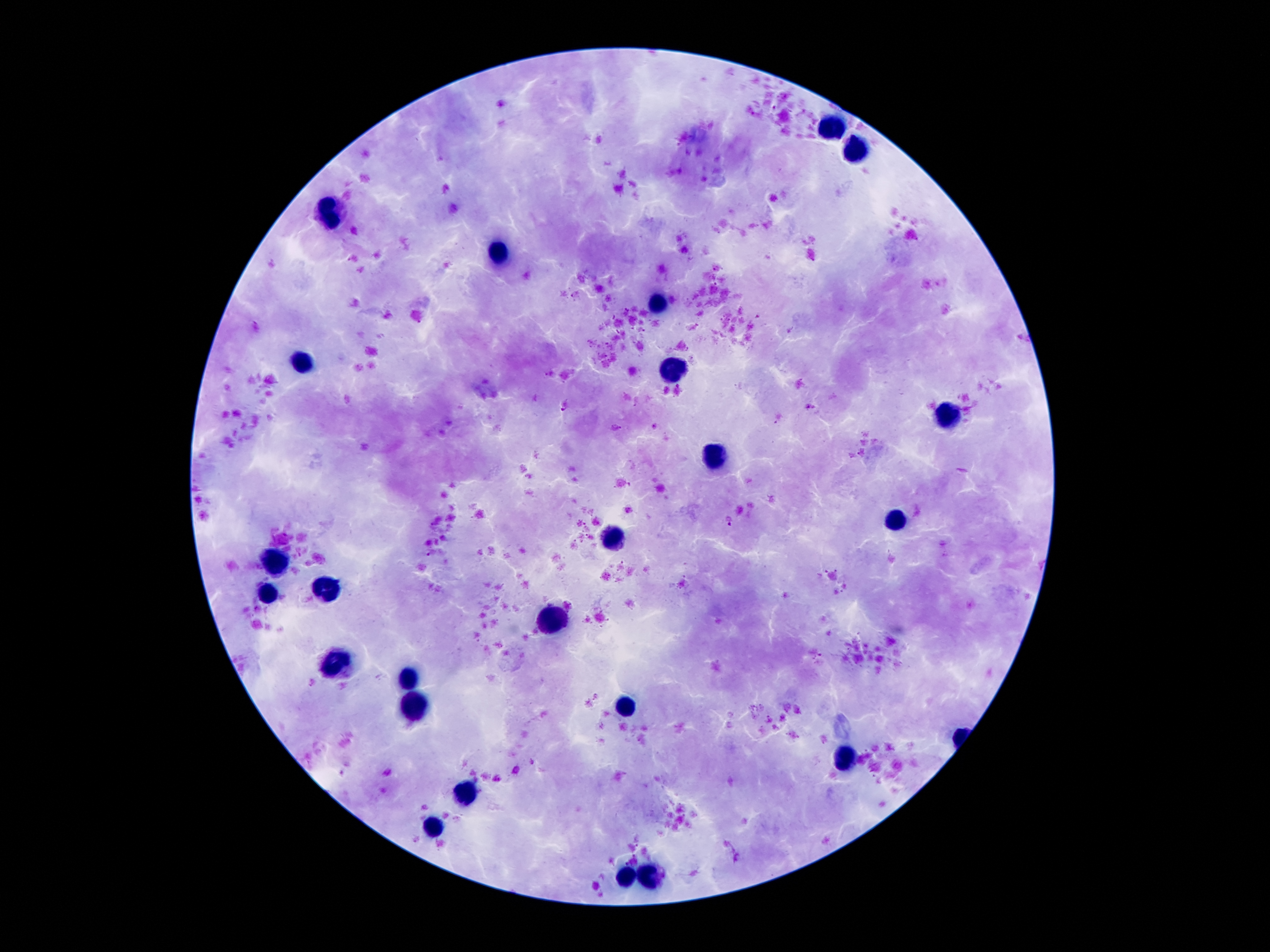
coordinate format = approximate centers as [x, y] in pixels
leukocyte locations = [833, 129], [854, 148], [329, 210], [497, 256], [659, 301], [304, 358], [674, 367], [947, 415], [713, 458], [892, 523], [609, 537], [275, 561], [325, 586], [266, 594], [554, 620], [336, 664], [409, 676], [627, 703], [413, 710], [845, 760], [463, 791], [431, 828], [624, 875], [649, 877]
Plasmodium parasite locations = [565, 406], [730, 521]
preparation = thick blood smear
patient malaria status = positive for Plasmodium falciparum
capture = smartphone camera through the microscope eyepiece
magnification = 100x
image size = 1270×952 pixels
stain = Giemsa
field of view = single